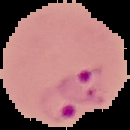

result: malaria parasites detected
image_type: segmented cell region on a black background
image_size: 130×130 pixels
preparation: thin blood smear